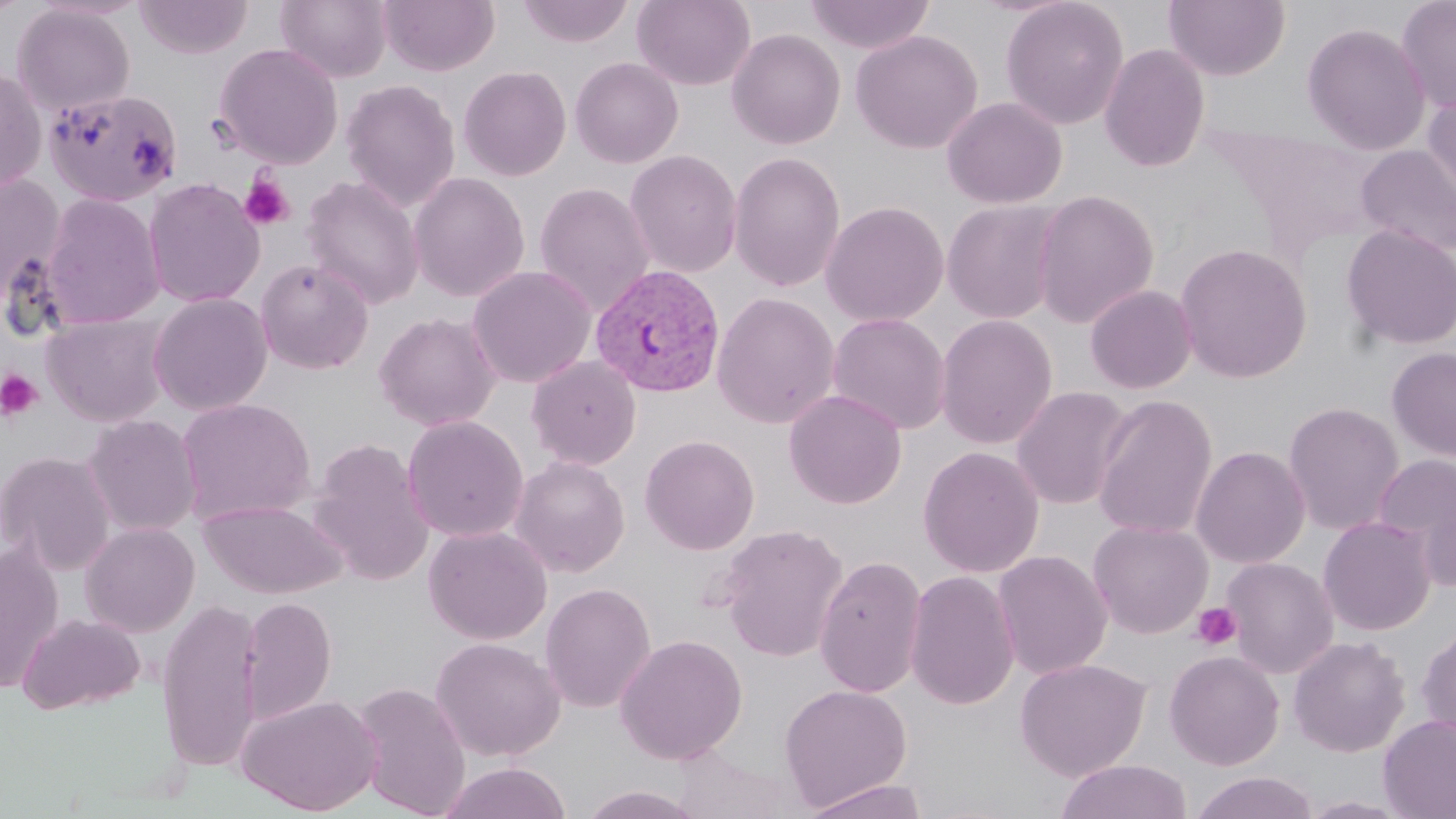
Summary:
  - Coordinate format: approximate bounding boxes as named x1/y1/x2/y2 corners in pixels
  - Plasmodium vivax-infected red blood cell locations: (x1=589, y1=262, x2=726, y2=397)
  - Platelet locations: (x1=239, y1=175, x2=295, y2=230), (x1=0, y1=369, x2=43, y2=421), (x1=1191, y1=602, x2=1242, y2=651)
  - Uninfected red blood cell locations: (x1=134, y1=0, x2=254, y2=59), (x1=274, y1=0, x2=392, y2=82), (x1=379, y1=0, x2=500, y2=76), (x1=517, y1=0, x2=635, y2=47), (x1=632, y1=0, x2=755, y2=90), (x1=804, y1=0, x2=935, y2=54), (x1=1000, y1=0, x2=1130, y2=130), (x1=1164, y1=0, x2=1290, y2=81), (x1=1395, y1=0, x2=1456, y2=114), (x1=12, y1=3, x2=136, y2=117), (x1=1301, y1=21, x2=1431, y2=155), (x1=726, y1=28, x2=846, y2=150), (x1=850, y1=29, x2=983, y2=154), (x1=214, y1=43, x2=344, y2=168), (x1=1099, y1=43, x2=1210, y2=172), (x1=569, y1=57, x2=684, y2=168), (x1=458, y1=65, x2=571, y2=181), (x1=0, y1=66, x2=48, y2=194), (x1=341, y1=79, x2=460, y2=211), (x1=1422, y1=87, x2=1456, y2=209), (x1=43, y1=88, x2=184, y2=208), (x1=942, y1=96, x2=1067, y2=209), (x1=1355, y1=144, x2=1456, y2=258), (x1=624, y1=150, x2=743, y2=278), (x1=728, y1=151, x2=846, y2=292), (x1=408, y1=172, x2=530, y2=302), (x1=0, y1=175, x2=67, y2=303), (x1=302, y1=175, x2=425, y2=310), (x1=143, y1=178, x2=265, y2=308), (x1=534, y1=182, x2=655, y2=315), (x1=1031, y1=189, x2=1159, y2=329), (x1=41, y1=194, x2=164, y2=329), (x1=941, y1=199, x2=1065, y2=324), (x1=820, y1=200, x2=949, y2=327), (x1=1340, y1=223, x2=1456, y2=351), (x1=1174, y1=243, x2=1312, y2=384), (x1=254, y1=258, x2=374, y2=375), (x1=466, y1=265, x2=596, y2=388), (x1=1085, y1=284, x2=1198, y2=394), (x1=712, y1=292, x2=841, y2=428), (x1=149, y1=293, x2=273, y2=415), (x1=41, y1=311, x2=173, y2=427), (x1=373, y1=311, x2=501, y2=432), (x1=827, y1=313, x2=951, y2=435), (x1=935, y1=314, x2=1058, y2=449), (x1=1386, y1=346, x2=1456, y2=463), (x1=527, y1=355, x2=642, y2=470), (x1=1011, y1=387, x2=1134, y2=509), (x1=784, y1=389, x2=907, y2=509), (x1=1092, y1=393, x2=1218, y2=541), (x1=177, y1=398, x2=316, y2=525), (x1=1282, y1=401, x2=1405, y2=535), (x1=82, y1=414, x2=202, y2=537), (x1=403, y1=415, x2=529, y2=542), (x1=640, y1=434, x2=759, y2=555), (x1=307, y1=438, x2=434, y2=586), (x1=1191, y1=445, x2=1310, y2=569), (x1=918, y1=446, x2=1044, y2=578), (x1=0, y1=451, x2=116, y2=574), (x1=1374, y1=454, x2=1456, y2=581), (x1=509, y1=455, x2=630, y2=578), (x1=197, y1=499, x2=347, y2=598), (x1=1318, y1=516, x2=1437, y2=636), (x1=1088, y1=520, x2=1213, y2=638), (x1=80, y1=522, x2=200, y2=637), (x1=716, y1=523, x2=849, y2=663), (x1=423, y1=524, x2=553, y2=645), (x1=0, y1=545, x2=64, y2=695), (x1=992, y1=549, x2=1112, y2=679), (x1=814, y1=554, x2=927, y2=698), (x1=1222, y1=557, x2=1339, y2=679), (x1=905, y1=570, x2=1020, y2=711), (x1=539, y1=582, x2=657, y2=713), (x1=239, y1=596, x2=336, y2=723), (x1=157, y1=598, x2=263, y2=774), (x1=17, y1=613, x2=145, y2=714), (x1=1416, y1=624, x2=1456, y2=743), (x1=614, y1=634, x2=748, y2=764), (x1=1288, y1=635, x2=1411, y2=757), (x1=430, y1=636, x2=565, y2=761), (x1=1164, y1=650, x2=1285, y2=770), (x1=1014, y1=657, x2=1151, y2=781), (x1=352, y1=680, x2=472, y2=818), (x1=779, y1=683, x2=912, y2=811), (x1=236, y1=693, x2=383, y2=815), (x1=1378, y1=714, x2=1456, y2=819), (x1=670, y1=748, x2=806, y2=819), (x1=1055, y1=759, x2=1192, y2=819), (x1=439, y1=762, x2=572, y2=819), (x1=1190, y1=771, x2=1318, y2=819), (x1=802, y1=778, x2=930, y2=818), (x1=577, y1=784, x2=708, y2=819), (x1=1299, y1=796, x2=1413, y2=818)
  - Slide-level diagnosis: Plasmodium vivax
  - Preparation: thin blood smear
  - Field of view: one of a larger specimen
  - Stain: May-Grünwald-Giemsa
  - Modality: light microscopy
  - Magnification: 1000x
  - Image size: 1456×819 pixels